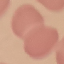
result: negative for malaria parasites
capture: smartphone through the microscope eyepiece
image_type: automatically extracted cell patch, resized to 64 × 64 pixels
preparation: thin blood smear
stain: Giemsa